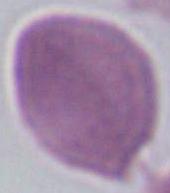
Summary:
  - Identification: erythrocyte
  - Magnification: 1000x
  - Modality: photomicrograph